Give the preparation type.
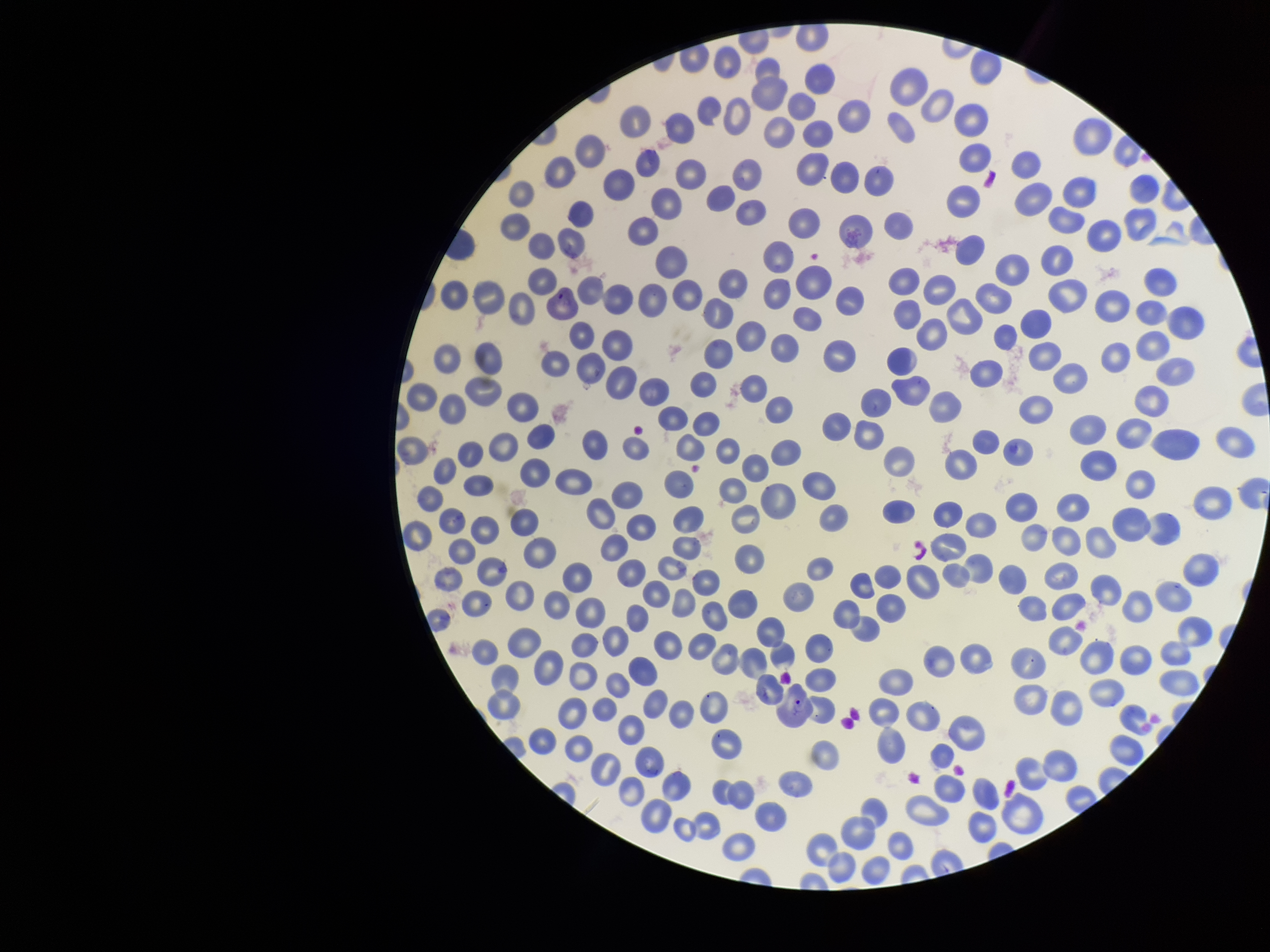
It is a thin blood smear.

Parasitized red blood cells: none seen. Single field of view. Patient malaria status: infected. Red blood cell count: 270. Giemsa stain. Image is 1270×952 pixels. Smartphone photograph taken through the eyepiece of a microscope. Species reported for this patient: Plasmodium vivax. Parasitized red blood cell count: 0.